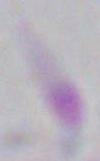
Summary:
  - Magnification: 1000x
  - Identification: Toxoplasma gondii
  - Modality: photomicrograph